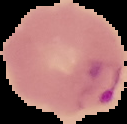

image size = 127×124 pixels
preparation = thin blood film
result = malaria parasites identified
image type = segmented cell region with the area outside set to black